State which parasite is depicted.
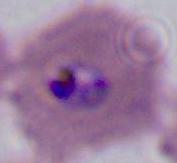
This is Plasmodium.

Summary:
  - Modality: photomicrograph
  - Magnification: 400x or 1000x